Locate and identify every blood parasite.
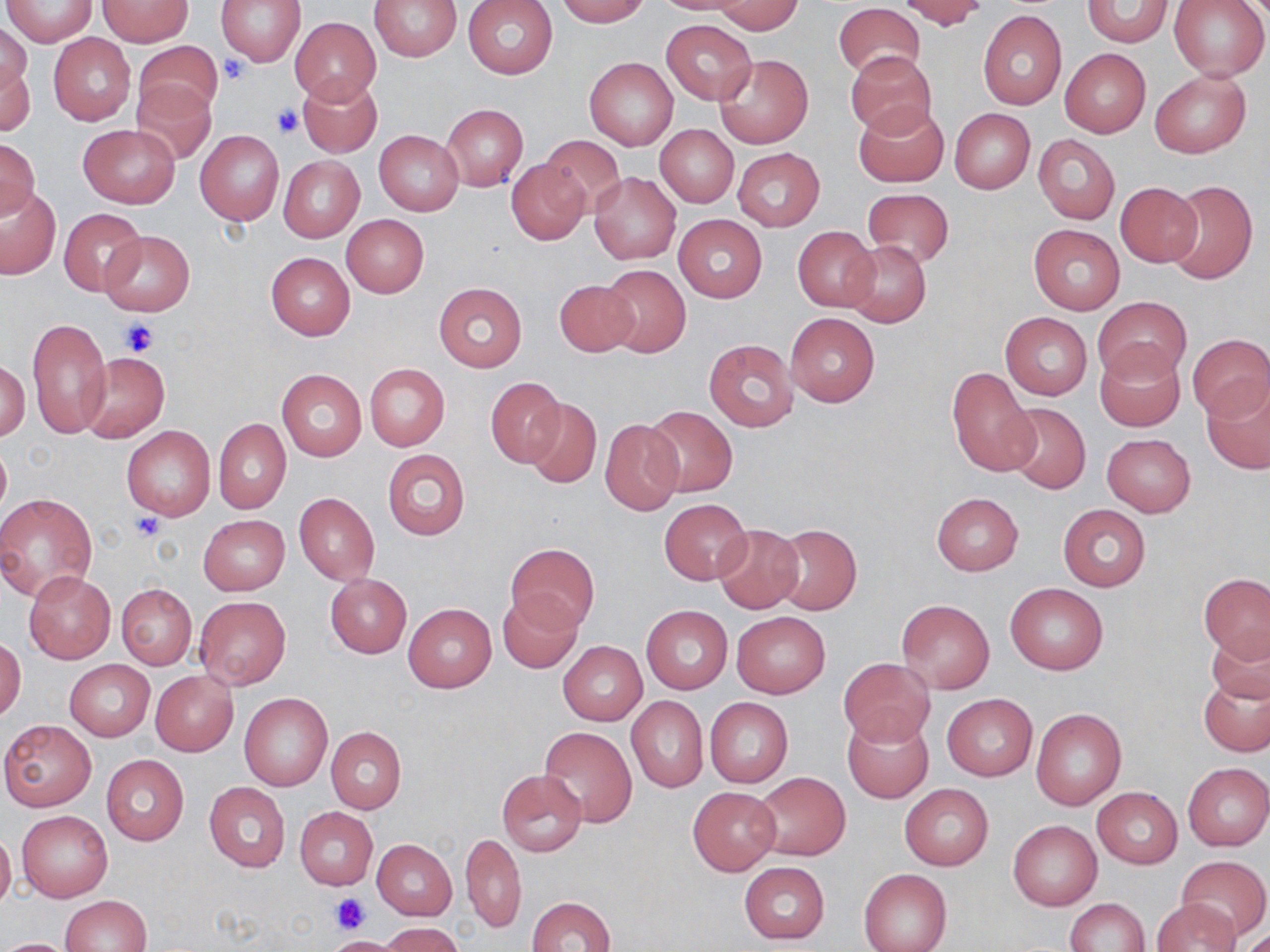

No blood parasites observed.

{
  "slide_level_diagnosis": "no evidence of blood parasites",
  "image_size": "1270×952 pixels",
  "field_of_view": "single",
  "modality": "light microscopy",
  "preparation": "thin blood film",
  "stain": "May-Grünwald-Giemsa",
  "uninfected_red_blood_cell_locations": "approximate bounding boxes as (x1,y1)-(x2,y2) corner pairs in pixels: (2,0)-(95,47), (215,0)-(306,65), (369,0)-(462,61), (555,0)-(652,25), (649,0)-(759,16), (900,0)-(986,29), (1083,0)-(1173,47), (1168,0)-(1269,80), (97,1)-(191,46), (463,1)-(557,78), (714,1)-(804,34), (833,3)-(926,80), (978,10)-(1066,110), (289,17)-(381,105), (661,19)-(757,103), (0,23)-(32,101), (48,34)-(135,125), (134,41)-(222,120), (1060,49)-(1150,137), (847,52)-(936,137), (714,53)-(813,149), (584,56)-(678,150), (3,61)-(35,140), (1149,70)-(1251,158), (296,74)-(382,158), (131,78)-(215,165), (853,102)-(949,188), (441,104)-(527,192), (949,108)-(1035,193), (78,124)-(180,207), (656,124)-(738,208), (195,130)-(284,225), (374,131)-(463,216), (540,135)-(627,217), (1033,135)-(1120,223), (0,137)-(40,218), (733,147)-(825,230), (277,155)-(364,243), (506,158)-(590,245), (589,172)-(681,265), (1163,179)-(1258,285), (1114,181)-(1203,266), (0,186)-(61,280), (862,188)-(954,267), (58,208)-(145,296), (340,214)-(428,298), (673,214)-(766,303), (1028,224)-(1124,314), (793,226)-(880,313), (98,231)-(194,316), (846,241)-(930,326), (265,252)-(355,339), (599,263)-(691,357), (552,278)-(639,357), (432,281)-(528,373), (1093,296)-(1191,382), (785,310)-(881,407), (1000,311)-(1092,400), (26,318)-(110,439), (1186,334)-(1270,423), (704,339)-(798,432), (1095,344)-(1186,432), (80,354)-(169,442), (0,360)-(30,442), (364,363)-(450,451), (947,367)-(1038,478), (276,369)-(366,462), (485,377)-(568,468), (1202,379)-(1270,476), (525,398)-(602,487), (1002,402)-(1090,493), (643,405)-(738,496), (213,417)-(291,513), (600,419)-(685,516), (121,425)-(216,520), (1102,433)-(1195,516), (0,439)-(10,521), (383,449)-(470,540), (931,492)-(1023,575), (0,493)-(98,601), (294,493)-(379,585), (660,498)-(750,583), (1058,504)-(1152,591), (198,515)-(289,595), (713,524)-(803,613), (771,524)-(862,615), (506,542)-(599,630), (23,572)-(115,664), (1200,573)-(1270,662), (325,574)-(411,658), (1004,582)-(1107,675), (116,584)-(196,669), (498,590)-(582,672), (194,595)-(291,691), (897,599)-(995,693), (403,603)-(496,693), (642,606)-(732,694), (732,613)-(830,698), (1206,628)-(1270,705), (0,637)-(26,722), (559,642)-(647,724), (839,658)-(934,745), (65,659)-(154,740), (1200,669)-(1270,758), (150,670)-(238,756), (941,691)-(1038,781), (240,692)-(333,790), (627,696)-(709,793), (704,698)-(793,787), (1031,707)-(1126,809), (842,713)-(934,804), (2,719)-(96,811), (539,725)-(637,827), (325,726)-(407,813), (101,754)-(189,846), (1183,762)-(1270,851), (496,769)-(586,856), (751,771)-(851,860), (204,782)-(290,873), (900,784)-(994,871), (687,786)-(780,875), (1092,788)-(1182,867), (296,807)-(377,889), (15,811)-(111,902), (1007,818)-(1102,911), (0,828)-(16,911), (462,832)-(526,933), (372,839)-(458,919), (1177,855)-(1269,941), (738,862)-(830,944), (859,869)-(952,952), (61,895)-(152,951), (528,895)-(615,952), (1064,898)-(1150,952), (1152,899)-(1240,952), (379,922)-(466,952), (327,936)-(402,952), (0,938)-(81,952)",
  "platelet_locations": "approximate bounding boxes as (x1,y1)-(x2,y2) corner pairs in pixels: (219,56)-(252,84), (272,105)-(302,138), (118,318)-(160,357), (131,513)-(165,541), (330,891)-(369,933)",
  "magnification": "1000x"
}